Locate every malaria parasite.
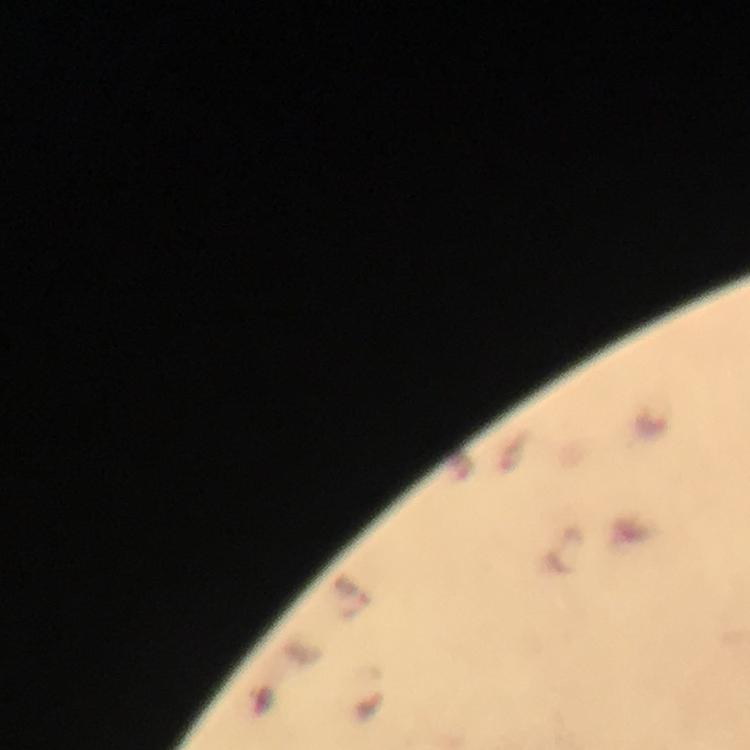
Approximate centers as [x, y] in pixels.
Malaria parasites: [652, 422].

Photographed through the microscope with a smartphone camera. Cropped region of a single field of view. Immersion oil was used. Thick blood smear. From a diagnostic examination for malaria. Giemsa stain. Image is 750×750 pixels. At 100x magnification.